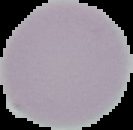
Summary:
  - Malaria status: uninfected
  - Preparation: thin blood film
  - Image type: segmented cell region on a black background
  - Image size: 133×130 pixels